Classify this cell by malaria status.
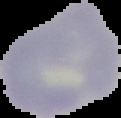

It is uninfected.

Image is 121×118 pixels. Cell region segmented out of the field of view; the surrounding area is masked to black. From a thin blood film.